Classify this cell by malaria status.
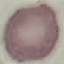
Uninfected.

Summary:
  - Stain: Giemsa
  - Preparation: thin blood film
  - Image type: cell patch, automatically extracted from a larger field of view and resized to 64 × 64 pixels
  - Capture: smartphone camera at the microscope eyepiece